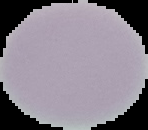
{
  "image_type": "segmented cell region with the area outside set to black",
  "preparation": "thin blood smear",
  "result": "no malaria parasites seen",
  "image_size": "148×130 pixels"
}